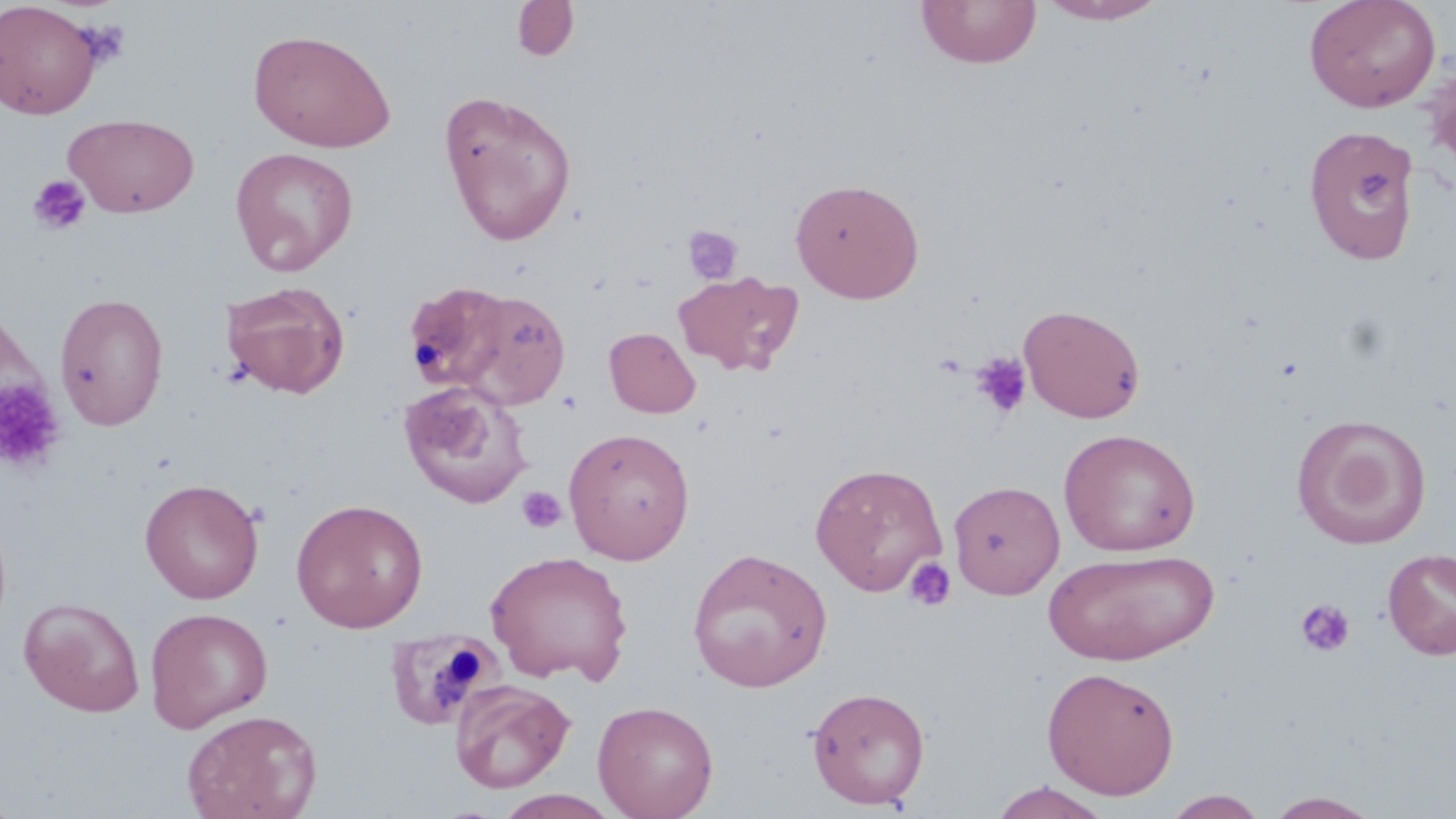
Approximate bounding boxes as named x1/y1/x2/y2 corners in pixels. Uninfected red blood cell locations: (x1=916, y1=0, x2=1041, y2=69), (x1=1036, y1=0, x2=1171, y2=25), (x1=1304, y1=0, x2=1441, y2=113), (x1=1, y1=1, x2=102, y2=120), (x1=511, y1=1, x2=579, y2=62), (x1=241, y1=28, x2=377, y2=274), (x1=248, y1=28, x2=396, y2=152), (x1=1423, y1=62, x2=1456, y2=176), (x1=438, y1=89, x2=577, y2=245), (x1=63, y1=113, x2=199, y2=218), (x1=1303, y1=124, x2=1422, y2=266), (x1=230, y1=146, x2=359, y2=275), (x1=790, y1=177, x2=925, y2=303), (x1=674, y1=270, x2=803, y2=375), (x1=220, y1=280, x2=351, y2=399), (x1=408, y1=281, x2=511, y2=396), (x1=455, y1=290, x2=570, y2=409), (x1=54, y1=292, x2=169, y2=430), (x1=1019, y1=303, x2=1146, y2=423), (x1=605, y1=327, x2=700, y2=417), (x1=399, y1=381, x2=534, y2=509), (x1=1292, y1=414, x2=1432, y2=549), (x1=563, y1=427, x2=695, y2=564), (x1=1059, y1=428, x2=1201, y2=556), (x1=809, y1=462, x2=947, y2=596), (x1=140, y1=478, x2=264, y2=604), (x1=948, y1=480, x2=1065, y2=599), (x1=290, y1=498, x2=429, y2=633), (x1=687, y1=547, x2=833, y2=692), (x1=1044, y1=548, x2=1218, y2=665), (x1=1383, y1=548, x2=1456, y2=660), (x1=485, y1=549, x2=633, y2=685), (x1=19, y1=597, x2=145, y2=717), (x1=145, y1=607, x2=273, y2=732), (x1=384, y1=631, x2=496, y2=731), (x1=1042, y1=665, x2=1180, y2=800), (x1=450, y1=679, x2=575, y2=794), (x1=807, y1=685, x2=930, y2=810), (x1=592, y1=700, x2=718, y2=819), (x1=181, y1=709, x2=322, y2=819), (x1=988, y1=781, x2=1114, y2=818), (x1=493, y1=789, x2=623, y2=818), (x1=1162, y1=790, x2=1269, y2=818), (x1=1264, y1=791, x2=1382, y2=818). Platelet locations: (x1=27, y1=174, x2=91, y2=235), (x1=681, y1=224, x2=744, y2=286), (x1=970, y1=352, x2=1032, y2=418), (x1=0, y1=380, x2=66, y2=474), (x1=517, y1=485, x2=566, y2=534), (x1=903, y1=556, x2=957, y2=612), (x1=1295, y1=599, x2=1356, y2=658). Slide-level diagnosis: negative for blood parasites. Thin blood smear. Image is 1456×819 pixels. Captured at 1000x magnification. Light microscopy. Single field of view. May-Grünwald-Giemsa-stained preparation.